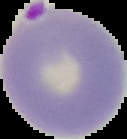 Malaria status: parasitized. Segmented cell region on a black background. From a thin blood film. Image is 127×139 pixels.